Report the malaria status of this cell.
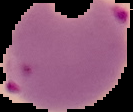
It is parasitized.

Summary:
  - Image size: 133×112 pixels
  - Image type: segmented cell region with the area outside set to black
  - Preparation: thin blood film